Assess this cell for malaria.
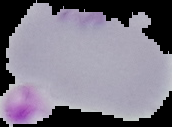

It is uninfected.

Summary:
  - Image size: 172×127 pixels
  - Preparation: thin blood film
  - Image type: segmented cell region on a black background